State the preparation type.
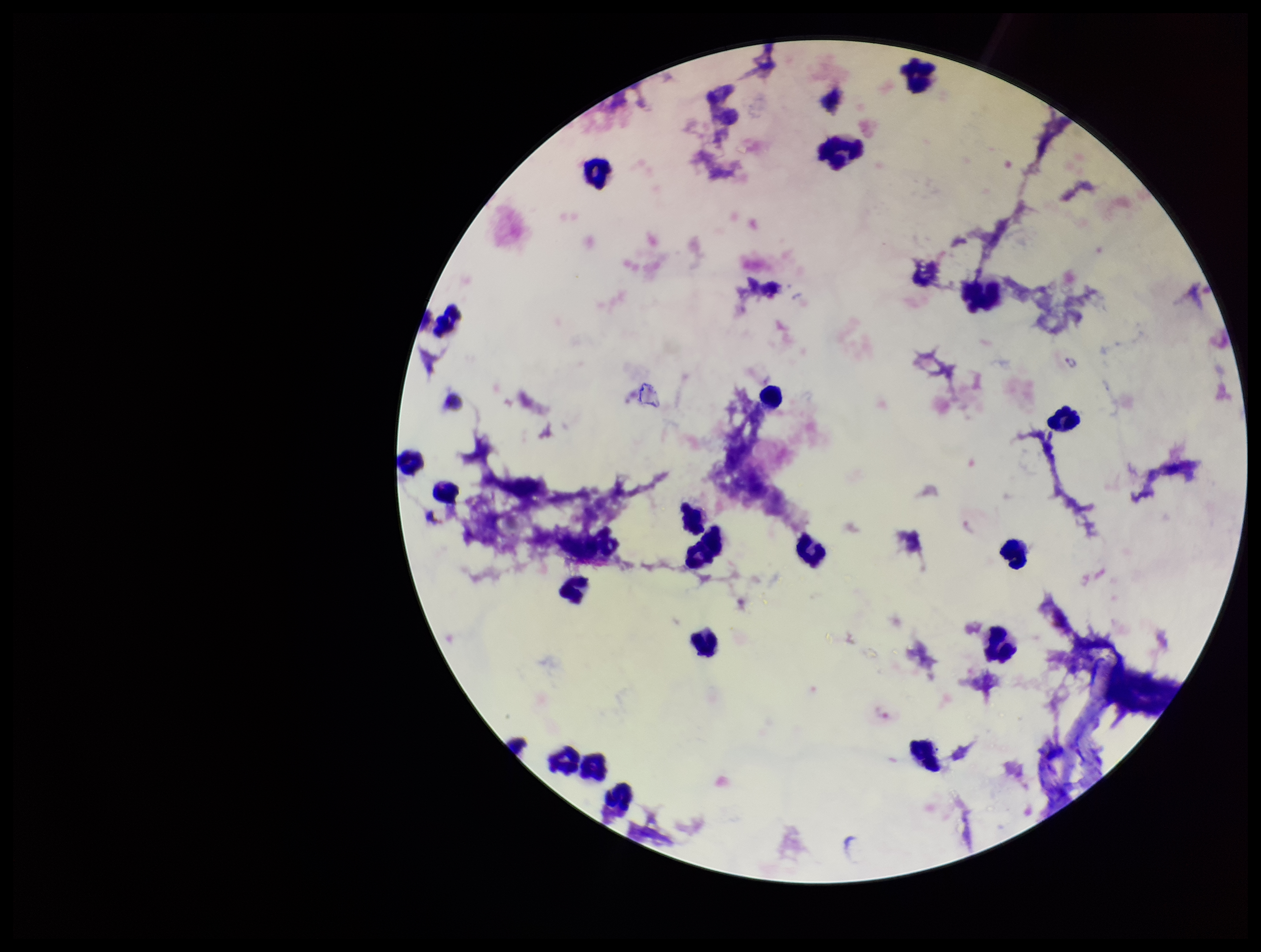

It is a thick blood smear.

stain = Giemsa
capture = smartphone photograph through the microscope eyepiece
Plasmodium parasites = seen
parasite count = 3
image size = 1261×952 pixels
field of view = single
patient malaria status = positive
leukocyte count = 23
species reported for this patient = Plasmodium vivax